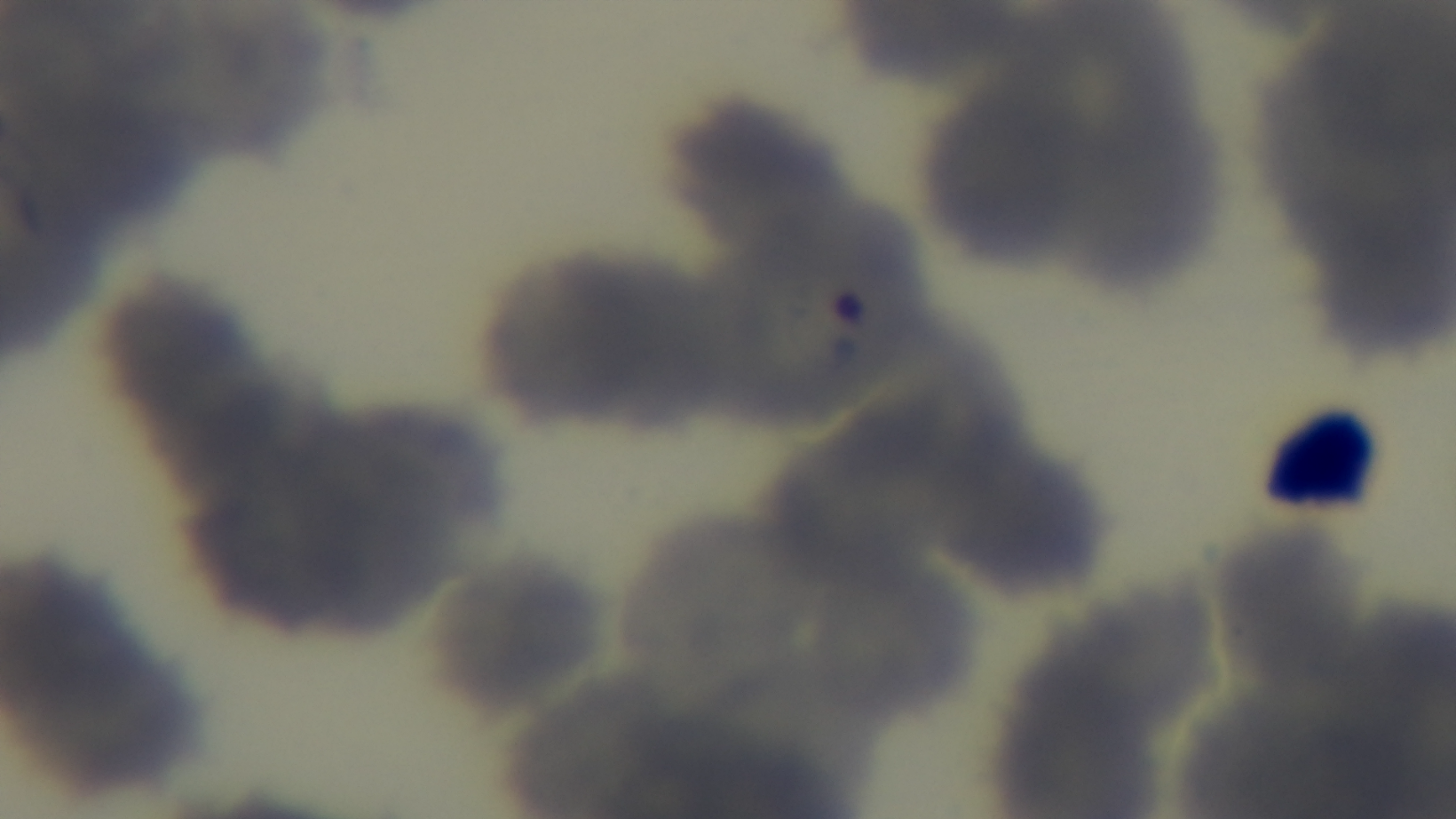 Oil-immersion objective, 100x. Captured with a mounted 4K digital camera. Preparation: thin smear. Giemsa stain. Malaria status: positive. Light microscopy. Single field of view.